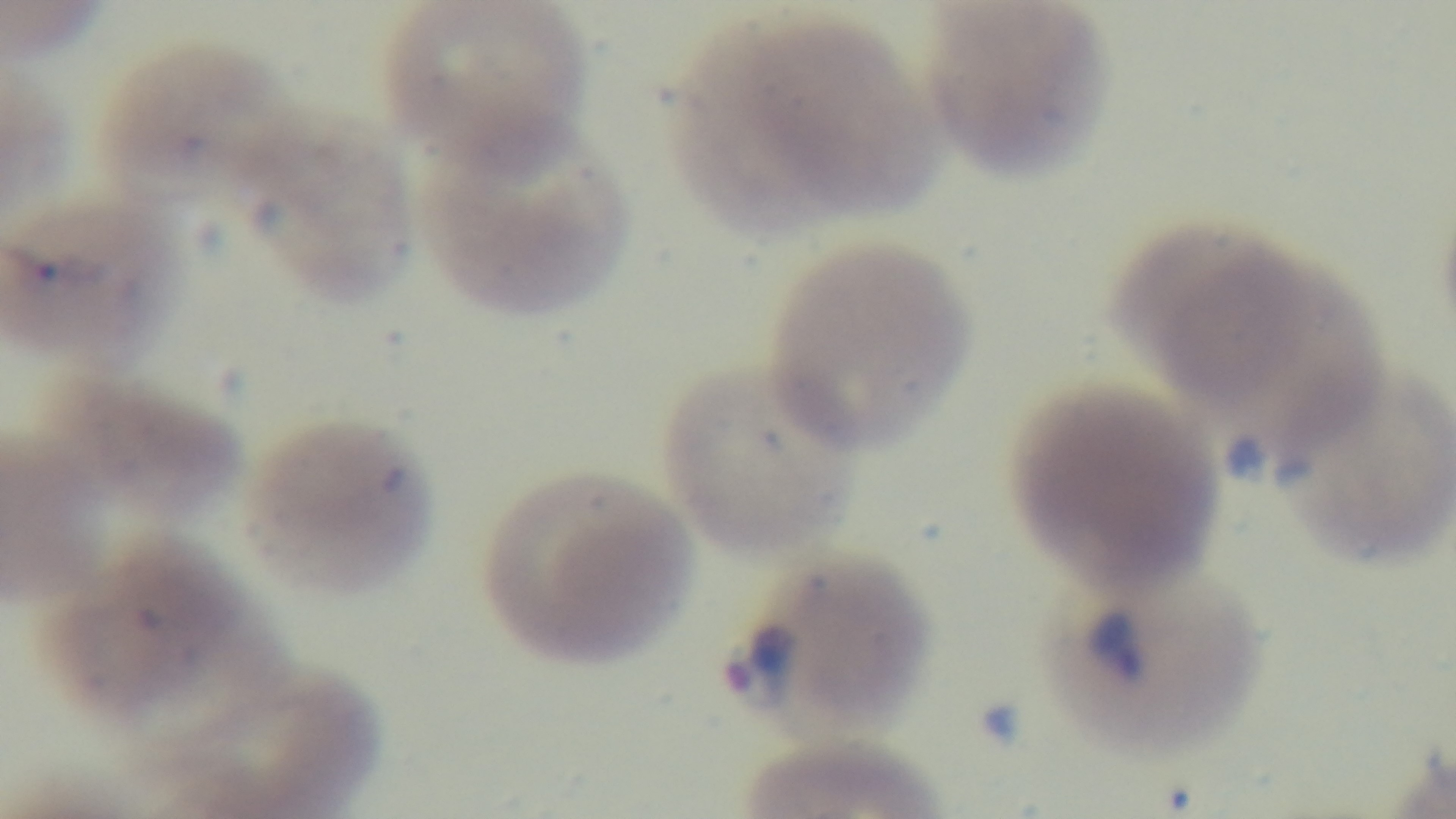
Summary:
  - Malaria status: positive
  - Capture: mounted 4K digital camera
  - Stain: Giemsa
  - Modality: light microscopy
  - Objective: 100x oil immersion
  - Field of view: one from the slide
  - Preparation: thin